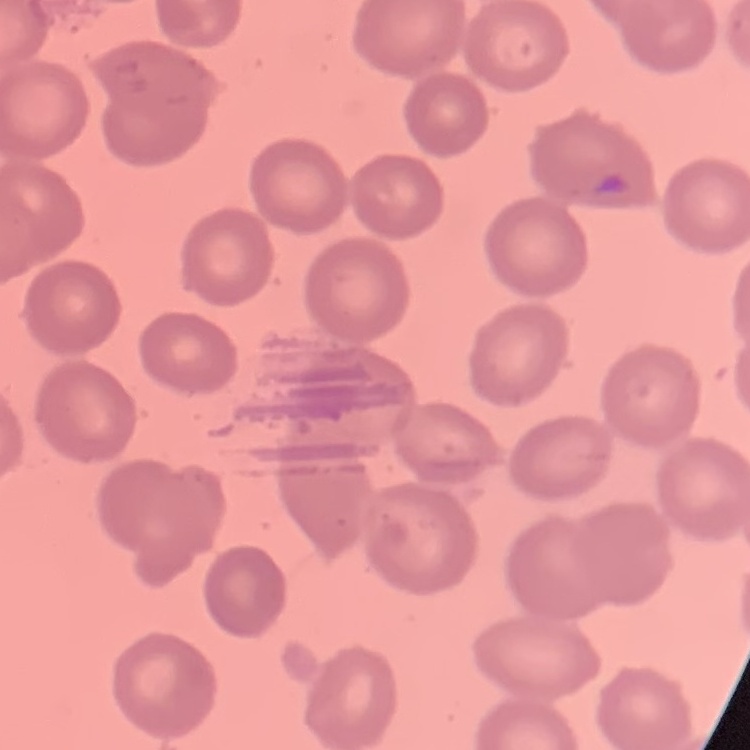
The erythrocytes show no rouleaux formation. One tile cut from a larger photomicrograph. Thin peripheral smear. Stained with either Field's or Giemsa.